Name the parasite shown.
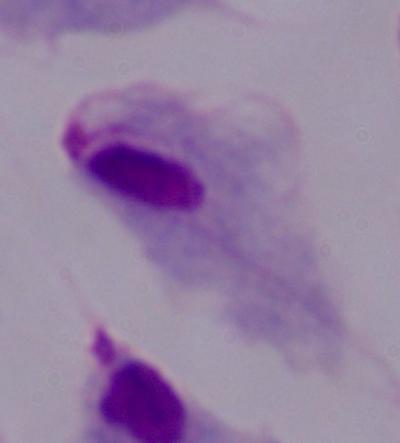
This is a trichomonad.

Photomicrograph. 1000x magnification.